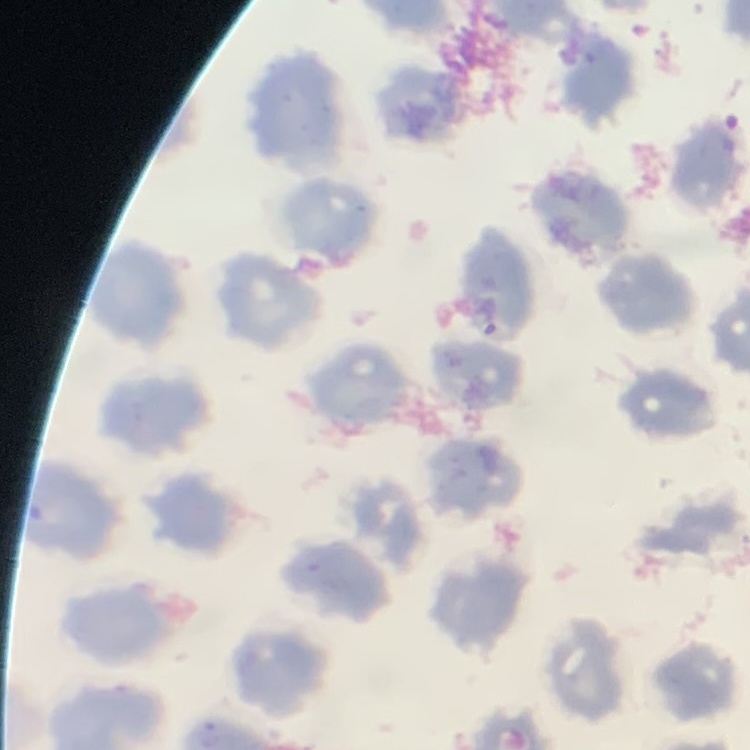

Summary:
  - Erythrocyte morphology: no rouleaux formation
  - Preparation: thin blood film
  - Stain: Field's or Giemsa
  - Image type: square crop of a larger photomicrograph